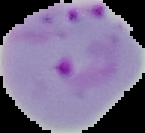
Malaria status: parasitized. Image is 145×133 pixels. Cell region segmented out of the field of view; the surrounding area is masked to black. From a thin blood film.